Mark where platelets are.
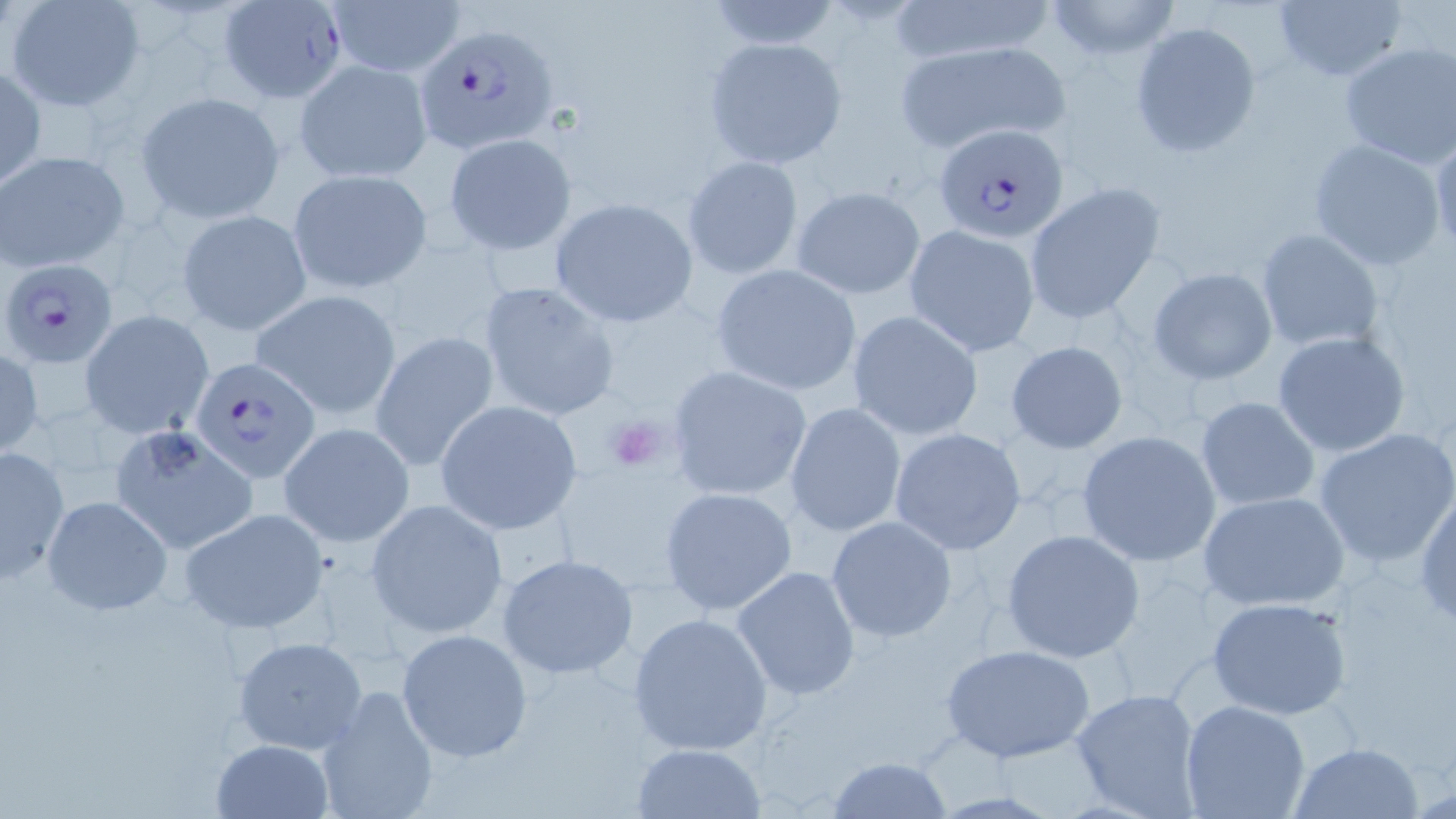
Approximate bounding boxes as (x1,y1)-(x2,y2) corner pairs in pixels.
Platelets: (601,411)-(673,476).

slide_level_diagnosis: Plasmodium falciparum
stain: May-Grünwald-Giemsa
field_of_view: one of a larger specimen
uninfected_red_blood_cell_locations: 'approximate bounding boxes as (x1,y1)-(x2,y2) corner pairs in pixels: (326,0)-(466,77), (701,0)-(847,52), (881,0)-(1060,67), (1043,0)-(1183,60), (7,1)-(146,112), (1272,1)-(1406,82), (1129,21)-(1259,158), (702,37)-(847,169), (892,38)-(1073,153), (1339,42)-(1456,168), (294,58)-(433,185), (0,63)-(45,189), (137,91)-(284,221), (1430,129)-(1456,256), (444,131)-(577,256), (1307,139)-(1446,270), (0,150)-(128,273), (681,155)-(805,280), (287,168)-(431,293), (1023,181)-(1166,325), (792,187)-(925,299), (549,199)-(699,326), (176,209)-(312,337), (904,225)-(1040,357), (1255,228)-(1385,353), (709,264)-(863,396), (1147,268)-(1278,385), (478,279)-(621,423), (251,289)-(402,418), (845,310)-(985,440), (81,312)-(213,437), (371,331)-(499,474), (1271,331)-(1409,458), (1005,340)-(1129,453), (0,346)-(42,458), (664,364)-(812,502), (1194,396)-(1321,512), (435,400)-(583,535), (786,402)-(907,537), (279,421)-(414,547), (110,422)-(258,555), (888,427)-(1027,555), (1314,427)-(1456,568), (1076,431)-(1222,567), (1,446)-(70,583), (659,487)-(797,615), (1414,488)-(1456,630), (1198,490)-(1351,611), (41,494)-(172,616), (366,498)-(509,640), (180,508)-(329,635), (826,516)-(959,643), (1001,528)-(1145,663), (498,555)-(638,680), (730,566)-(860,701), (1206,595)-(1353,719), (627,612)-(775,757), (396,628)-(533,763), (231,636)-(367,754), (939,643)-(1097,764), (315,685)-(439,819), (1070,688)-(1203,817), (1180,700)-(1310,819), (211,738)-(334,819), (631,741)-(765,817), (1289,741)-(1424,818), (827,756)-(953,818)'
image_size: 1456×819 pixels
modality: optical microscopy
preparation: thin blood film
magnification: 1000x
plasmodium_falciparum_infected_red_blood_cell_locations: 'approximate bounding boxes as (x1,y1)-(x2,y2) corner pairs in pixels: (219,1)-(346,100), (416,22)-(561,152), (936,123)-(1069,242), (3,257)-(120,366), (189,355)-(320,483)'